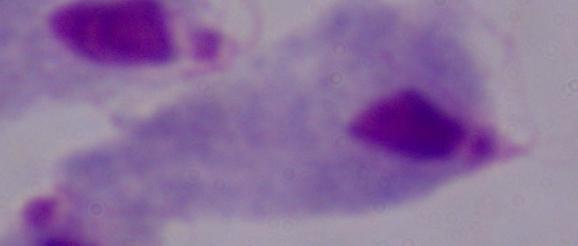
Summary:
  - Modality: photomicrograph
  - Magnification: 1000x
  - Identification: trichomonad